Identify the parasite.
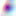

Toxoplasma gondii.

400x magnification. Photomicrograph.